Identify the parasite.
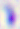

This is Toxoplasma gondii.

{
  "magnification": "400x",
  "modality": "photomicrograph"
}